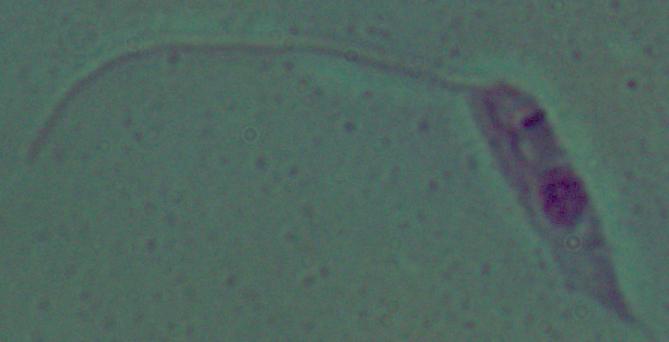

Photomicrograph. A Leishmania parasite is seen. Captured at 1000x magnification.